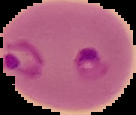
{
  "image_type": "cell region segmented out of the field of view; surrounding area masked to black",
  "preparation": "thin blood smear",
  "image_size": "136×115 pixels",
  "result": "Plasmodium parasites detected"
}